Classify this cell by malaria status.
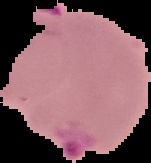

Parasitized.

Segmented cell region on a black background. Image is 151×163 pixels. From a thin blood film.